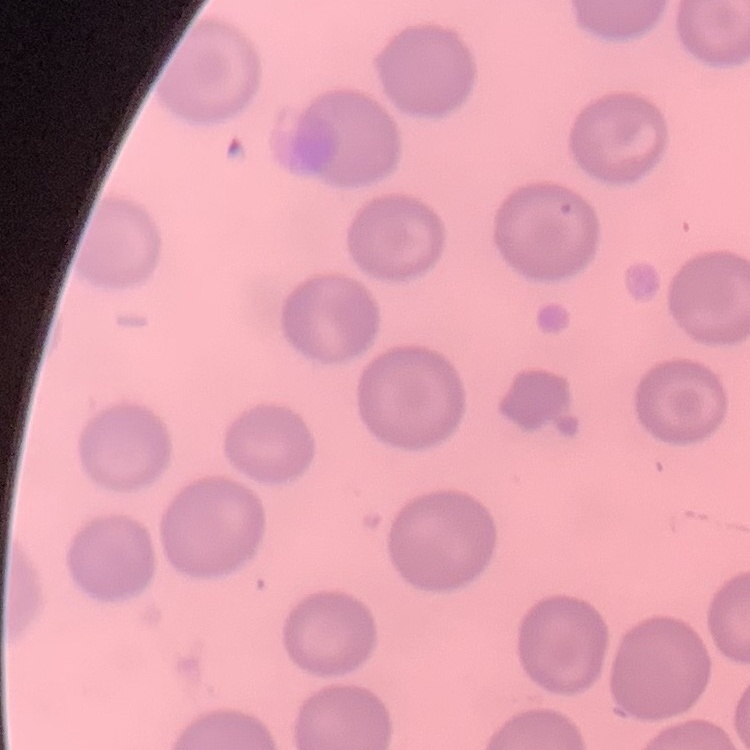

The red blood cells show no rouleaux formation. Square crop of a larger photomicrograph. Stained with either Field's or Giemsa. Thin blood film.